Report the malaria status of this cell.
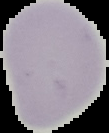
Uninfected.

image size = 109×133 pixels
preparation = thin blood film
image type = segmented cell region with the area outside set to black